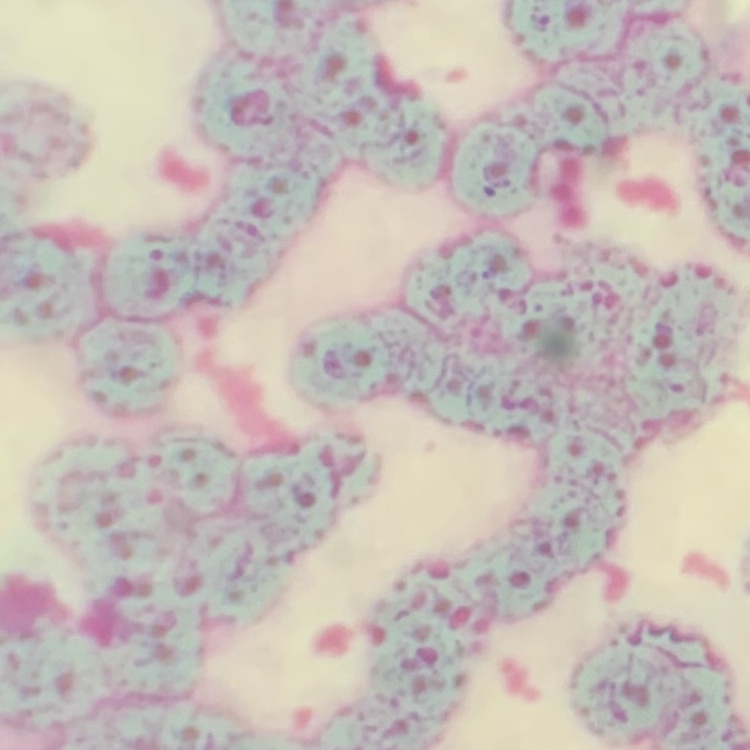

erythrocyte morphology = rouleaux formation
stain = Field's or Giemsa
image type = square crop of a larger photomicrograph
preparation = thin blood film